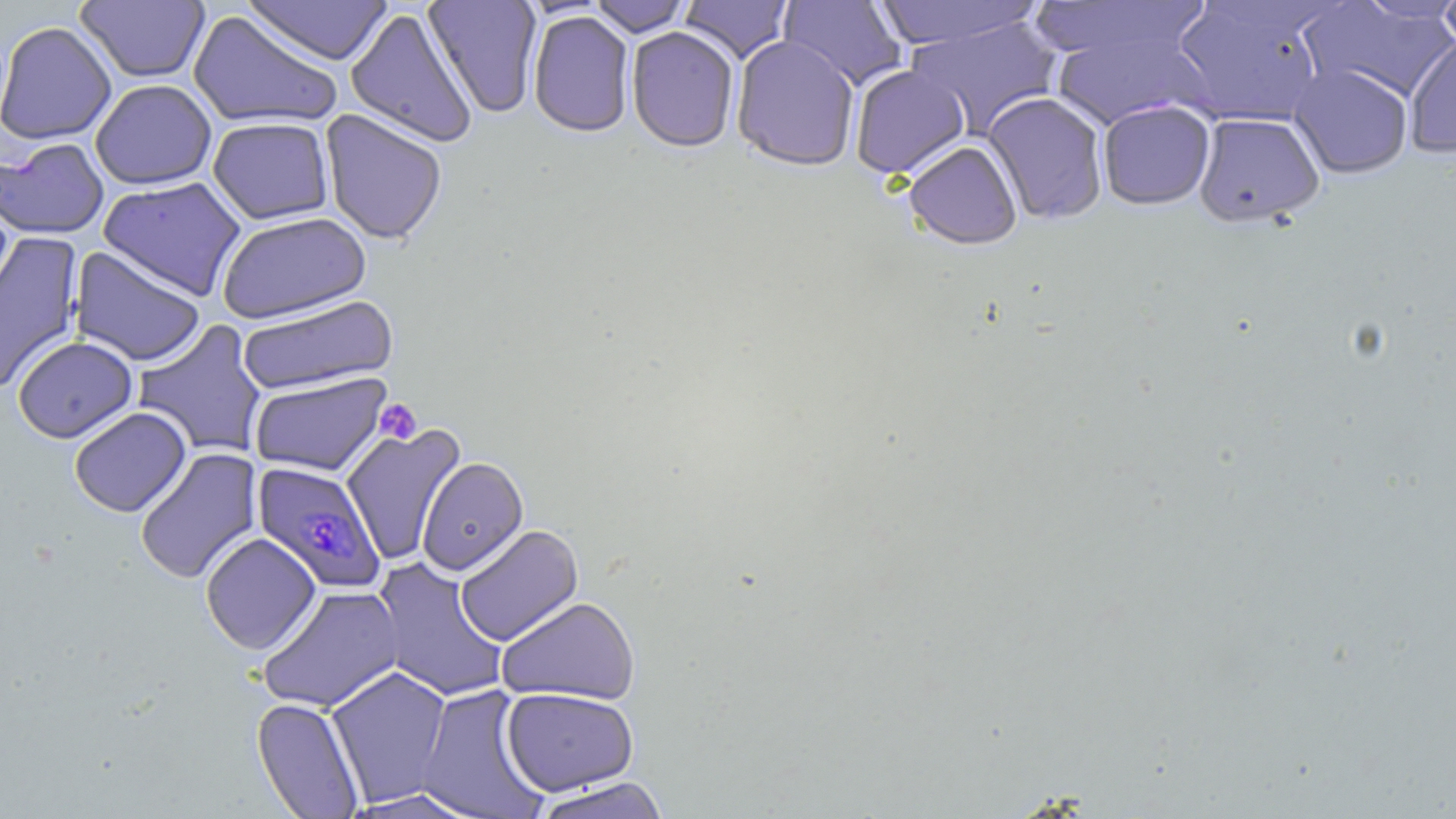
Approximate bounding boxes as (x1,y1)-(x2,y2) corner pairs in pixels. Platelet locations: (375,399)-(422,445). Plasmodium falciparum-infected red blood cell locations: (253,461)-(385,593). Uninfected red blood cell locations: (75,0)-(210,84), (241,0)-(394,66), (588,0)-(691,38), (679,0)-(795,65), (779,0)-(906,91), (873,0)-(1044,52), (1030,0)-(1214,68), (1169,0)-(1332,127), (1437,0)-(1456,57), (423,1)-(543,117), (1298,1)-(1456,105), (345,8)-(478,149), (188,10)-(342,131), (528,12)-(634,139), (905,17)-(1063,137), (0,21)-(117,145), (1048,22)-(1211,132), (626,28)-(740,155), (1404,34)-(1456,159), (731,36)-(860,174), (1289,64)-(1413,179), (850,65)-(970,180), (90,79)-(217,190), (982,91)-(1109,226), (1098,100)-(1216,211), (320,110)-(447,246), (1192,112)-(1325,229), (208,117)-(334,225), (0,138)-(109,240), (903,142)-(1023,251), (98,176)-(246,301), (216,211)-(371,325), (0,232)-(83,393), (69,246)-(206,367), (236,295)-(398,396), (132,320)-(268,458), (13,335)-(137,443), (250,372)-(391,476), (69,406)-(191,517), (341,422)-(466,565), (134,447)-(262,586), (416,457)-(529,575), (454,524)-(583,646), (200,532)-(321,655), (371,558)-(510,702), (256,584)-(404,713), (496,596)-(641,705), (325,665)-(453,808), (415,685)-(550,819), (501,688)-(639,796), (251,697)-(365,818), (530,777)-(673,819), (340,788)-(482,818). Slide-level diagnosis: Plasmodium falciparum. One field of a larger specimen. Light microscopy. Captured at 1000x magnification. Thin blood film. May-Grünwald-Giemsa-stained preparation. Image is 1456×819 pixels.